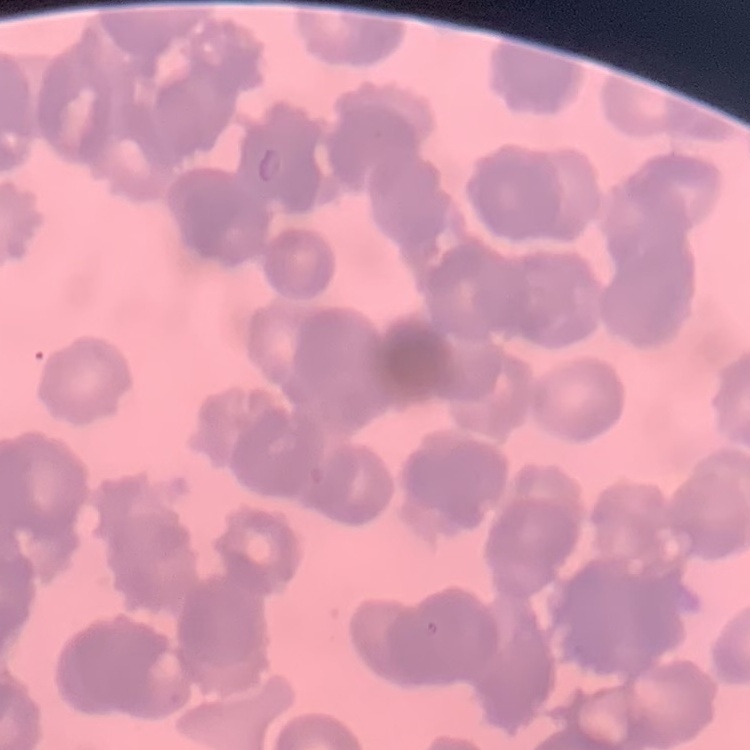
The erythrocytes exhibit rouleaux formation. Thin blood film. Stained with either Field's or Giemsa. One tile cut from a larger photomicrograph.